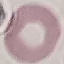

{
  "result": "negative for malaria parasites",
  "stain": "Giemsa",
  "image_type": "cell patch, automatically extracted from a larger field of view and resized to 64 × 64 pixels",
  "preparation": "thin smear",
  "capture": "smartphone camera at the microscope eyepiece"
}